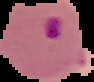

image size = 94×82 pixels
result = malaria parasites identified
image type = segmented cell region with the area outside set to black
preparation = thin blood smear